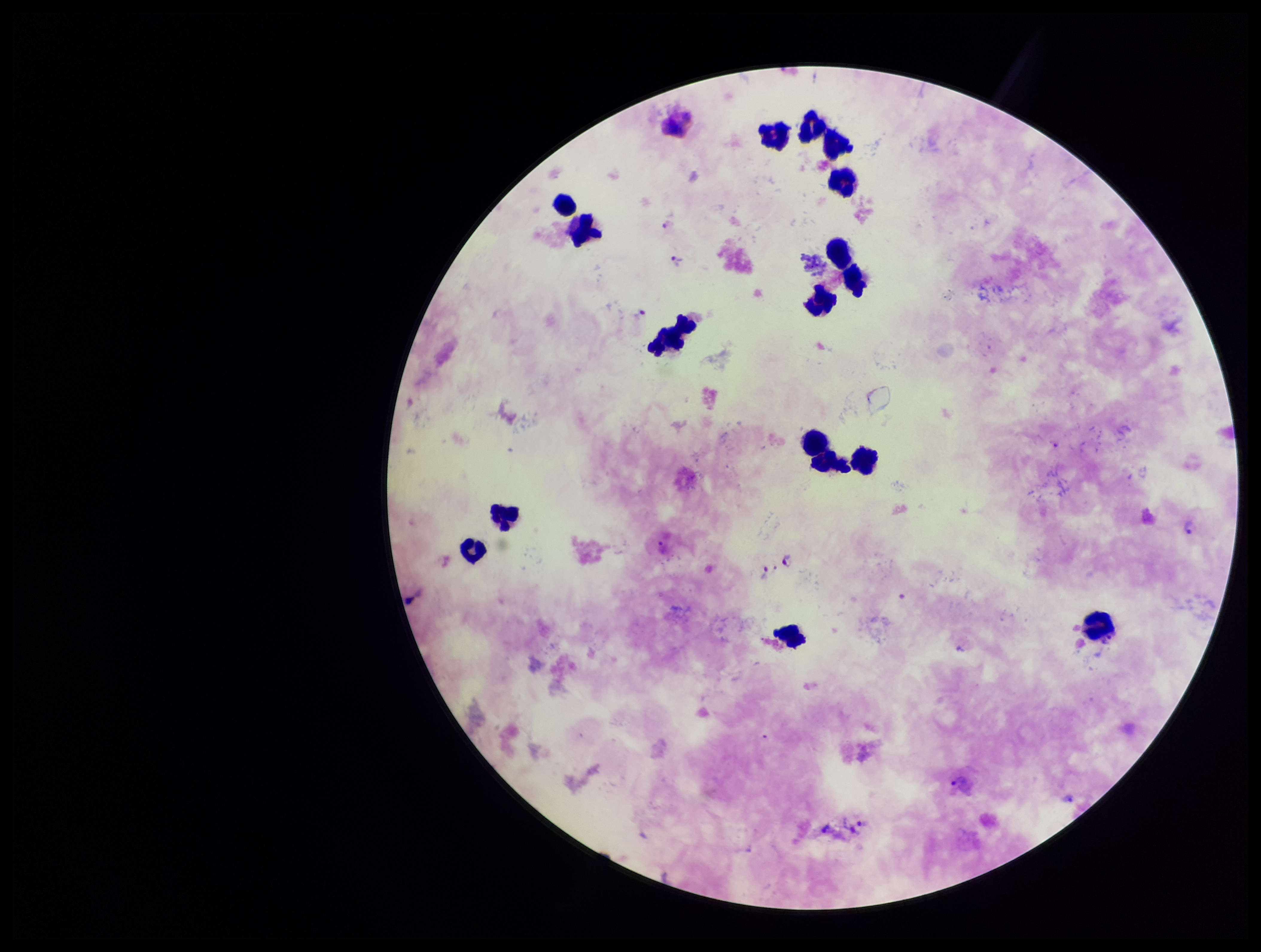 Plasmodium parasites: detected. Image is 1261×952 pixels. Species reported for this patient: Plasmodium vivax. Smartphone photograph taken through the eyepiece of a microscope. Leukocyte count: 16. Stained with Giemsa. Parasite count: 11. Preparation: thick. Patient malaria status: infected. One field from this slide.